Point out each malaria parasite and each leukocyte.
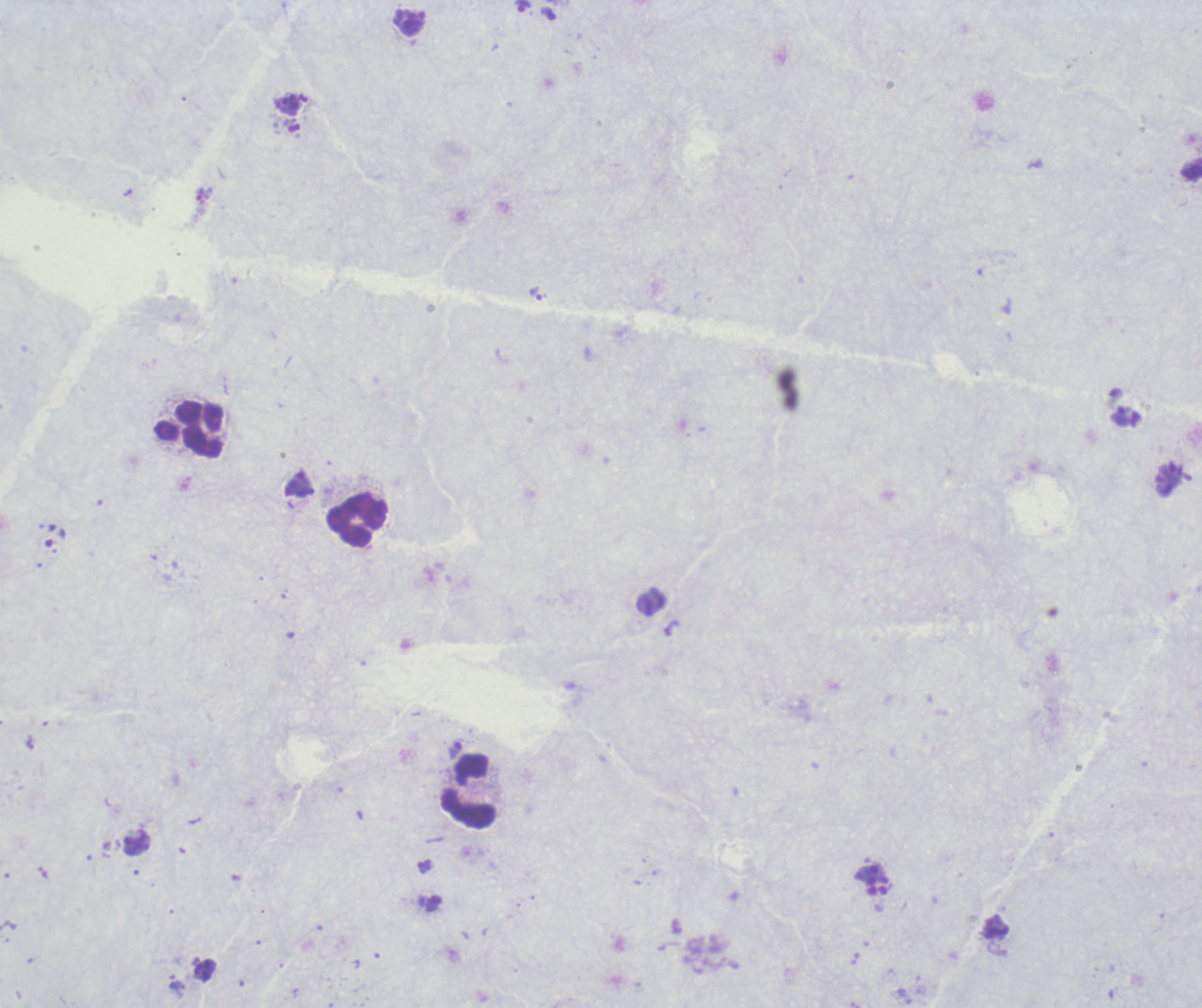

Approximate centers as [x, y] in pixels.
Trophozoites: [535, 294], [1121, 416].
Schizonts: [872, 880].
No gametocyte forms observed.
Leukocytes: [189, 430], [358, 519], [470, 792].

Summary:
  - Context: previously used in an actual diagnosis
  - Field of view: one from this slide
  - Magnification: 100x
  - Background quality: poor
  - Stain: Romanowsky
  - Image size: 1202×1008 pixels
  - Preparation: thick smear of blood